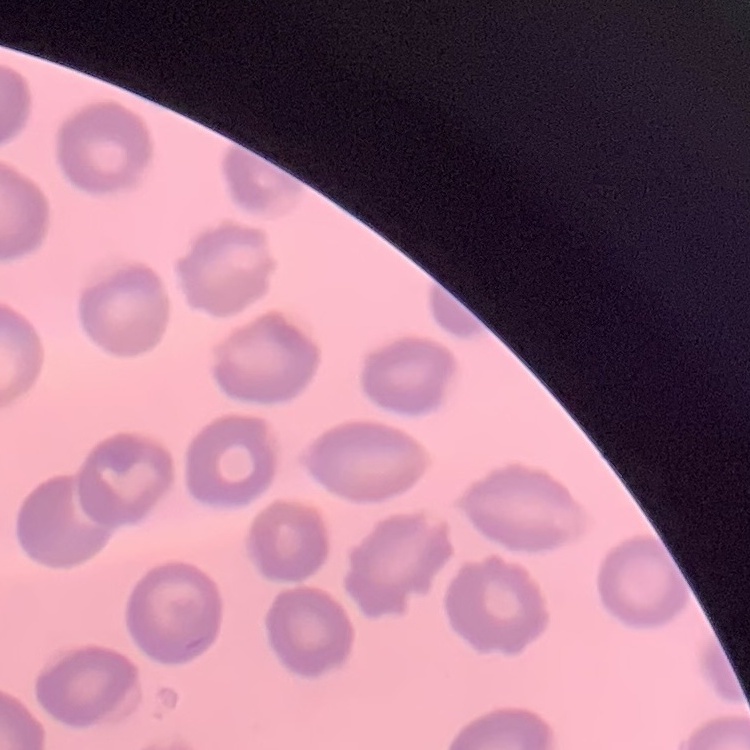
Summary:
  - Red blood cell morphology: no rouleaux formation
  - Preparation: thin peripheral smear
  - Image type: one tile cut from a larger photomicrograph
  - Stain: Field's or Giemsa